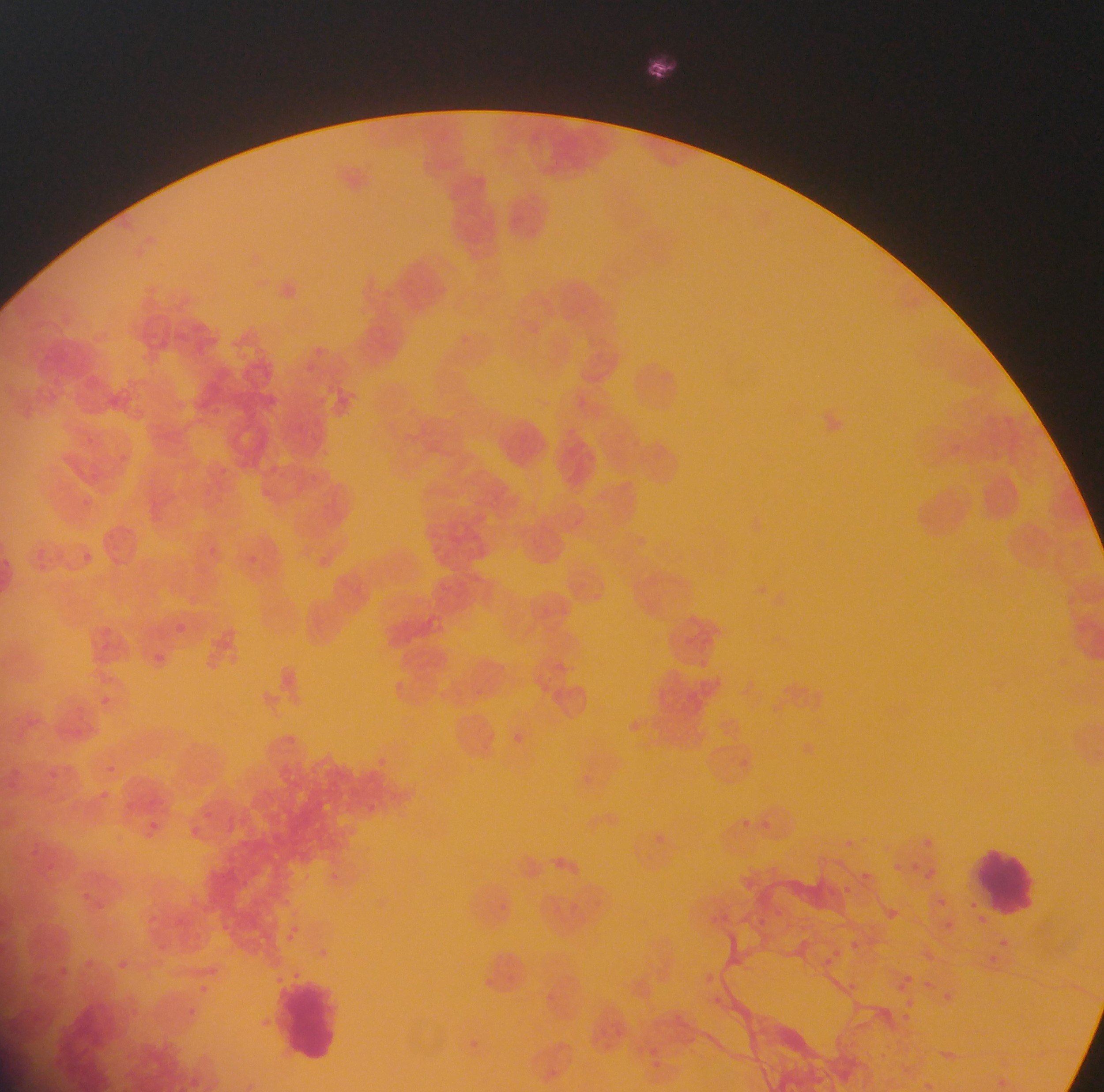
image size = 1104×1092 pixels
leukocyte locations = approximate bounding boxes as left top right bottom in pixels: 964 842 1048 925; 281 978 341 1069
capture = mobile-phone photograph through a microscope
field of view = single
preparation = thin blood film
Plasmodium parasite locations = approximate bounding boxes as left top right bottom in pixels: 513 732 531 748; 367 799 388 820; 738 817 760 835; 760 818 777 834; 926 834 934 846; 890 858 902 871; 927 865 943 882; 855 866 875 885; 333 871 346 883; 843 884 853 896; 939 897 949 907; 880 903 904 926; 774 907 785 922; 942 918 952 931; 289 925 305 937; 851 937 869 954; 998 938 1016 948; 831 947 846 961; 985 953 1000 968; 111 956 132 975; 902 969 914 981; 195 981 211 994; 842 983 858 991; 943 990 952 1006; 901 998 912 1012; 184 1003 201 1019
country = Ghana